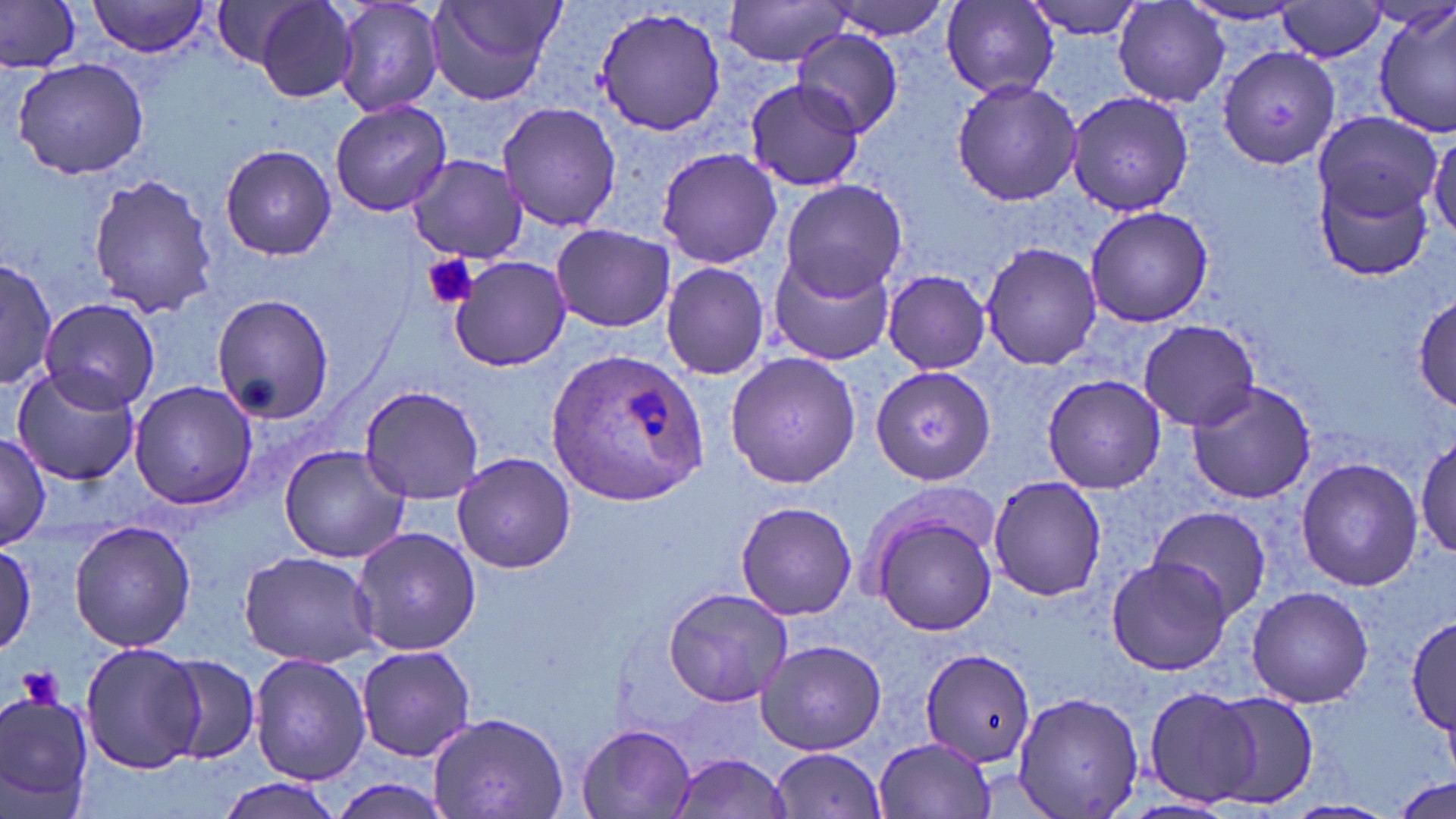
Approximate bounding boxes as named x1/y1/x2/y2 corners in pixels. Plasmodium ovale-infected red blood cell locations: (x1=547, y1=347, x2=707, y2=502). Platelet locations: (x1=423, y1=253, x2=480, y2=310), (x1=18, y1=667, x2=65, y2=711). Uninfected red blood cell locations: (x1=86, y1=0, x2=215, y2=57), (x1=249, y1=0, x2=362, y2=103), (x1=331, y1=0, x2=446, y2=118), (x1=426, y1=0, x2=565, y2=106), (x1=722, y1=0, x2=853, y2=66), (x1=825, y1=0, x2=954, y2=40), (x1=1022, y1=0, x2=1151, y2=38), (x1=0, y1=1, x2=80, y2=72), (x1=210, y1=1, x2=314, y2=72), (x1=941, y1=1, x2=1060, y2=99), (x1=1114, y1=2, x2=1228, y2=106), (x1=1276, y1=2, x2=1389, y2=61), (x1=1179, y1=3, x2=1311, y2=29), (x1=592, y1=5, x2=731, y2=138), (x1=1374, y1=7, x2=1455, y2=138), (x1=792, y1=29, x2=903, y2=138), (x1=1220, y1=45, x2=1341, y2=172), (x1=12, y1=58, x2=150, y2=180), (x1=744, y1=78, x2=865, y2=192), (x1=951, y1=78, x2=1082, y2=206), (x1=1064, y1=88, x2=1196, y2=216), (x1=329, y1=99, x2=452, y2=217), (x1=496, y1=101, x2=623, y2=231), (x1=1312, y1=111, x2=1443, y2=225), (x1=1428, y1=129, x2=1456, y2=239), (x1=219, y1=144, x2=337, y2=261), (x1=656, y1=145, x2=781, y2=270), (x1=406, y1=154, x2=527, y2=264), (x1=1316, y1=168, x2=1437, y2=283), (x1=87, y1=172, x2=221, y2=319), (x1=778, y1=179, x2=909, y2=300), (x1=1085, y1=205, x2=1212, y2=327), (x1=550, y1=223, x2=676, y2=333), (x1=979, y1=242, x2=1105, y2=371), (x1=767, y1=248, x2=897, y2=367), (x1=449, y1=254, x2=572, y2=373), (x1=1, y1=258, x2=57, y2=388), (x1=660, y1=260, x2=771, y2=381), (x1=881, y1=270, x2=991, y2=374), (x1=1413, y1=290, x2=1454, y2=411), (x1=210, y1=291, x2=334, y2=425), (x1=41, y1=296, x2=163, y2=417), (x1=1137, y1=319, x2=1260, y2=431), (x1=724, y1=351, x2=860, y2=490), (x1=867, y1=364, x2=997, y2=485), (x1=11, y1=368, x2=140, y2=487), (x1=1041, y1=373, x2=1168, y2=495), (x1=128, y1=381, x2=258, y2=509), (x1=1186, y1=381, x2=1318, y2=503), (x1=357, y1=385, x2=484, y2=503), (x1=1415, y1=433, x2=1455, y2=562), (x1=0, y1=435, x2=50, y2=550), (x1=279, y1=445, x2=410, y2=564), (x1=450, y1=454, x2=577, y2=573), (x1=1293, y1=457, x2=1424, y2=591), (x1=988, y1=475, x2=1108, y2=601), (x1=862, y1=497, x2=1000, y2=640), (x1=734, y1=500, x2=858, y2=621), (x1=1147, y1=506, x2=1273, y2=620), (x1=69, y1=519, x2=197, y2=652), (x1=351, y1=527, x2=480, y2=655), (x1=0, y1=544, x2=36, y2=657), (x1=238, y1=550, x2=380, y2=668), (x1=1107, y1=557, x2=1234, y2=676), (x1=658, y1=584, x2=795, y2=710), (x1=1246, y1=585, x2=1375, y2=709), (x1=1405, y1=618, x2=1455, y2=736), (x1=755, y1=639, x2=886, y2=755), (x1=78, y1=641, x2=206, y2=773), (x1=355, y1=644, x2=478, y2=762), (x1=919, y1=648, x2=1037, y2=769), (x1=249, y1=653, x2=372, y2=786), (x1=163, y1=657, x2=259, y2=765), (x1=1142, y1=685, x2=1266, y2=807), (x1=1013, y1=688, x2=1143, y2=817), (x1=1205, y1=690, x2=1321, y2=810), (x1=0, y1=692, x2=97, y2=817), (x1=427, y1=708, x2=568, y2=819), (x1=573, y1=722, x2=699, y2=819), (x1=872, y1=736, x2=1000, y2=818), (x1=767, y1=749, x2=889, y2=817), (x1=668, y1=752, x2=795, y2=818), (x1=1393, y1=776, x2=1454, y2=817), (x1=215, y1=777, x2=344, y2=819), (x1=1283, y1=799, x2=1398, y2=819). Slide-level diagnosis: Plasmodium ovale. Image is 1456×819 pixels. 1000x magnification. Single field of view. Thin blood smear. May-Grünwald-Giemsa stain. Optical microscopy.